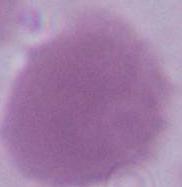
modality = micrograph
magnification = 1000x
identification = erythrocyte